Report the malaria status of this cell.
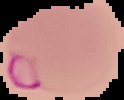
It is parasitized.

Summary:
  - Image size: 124×100 pixels
  - Image type: segmented cell region with the area outside set to black
  - Preparation: thin blood film